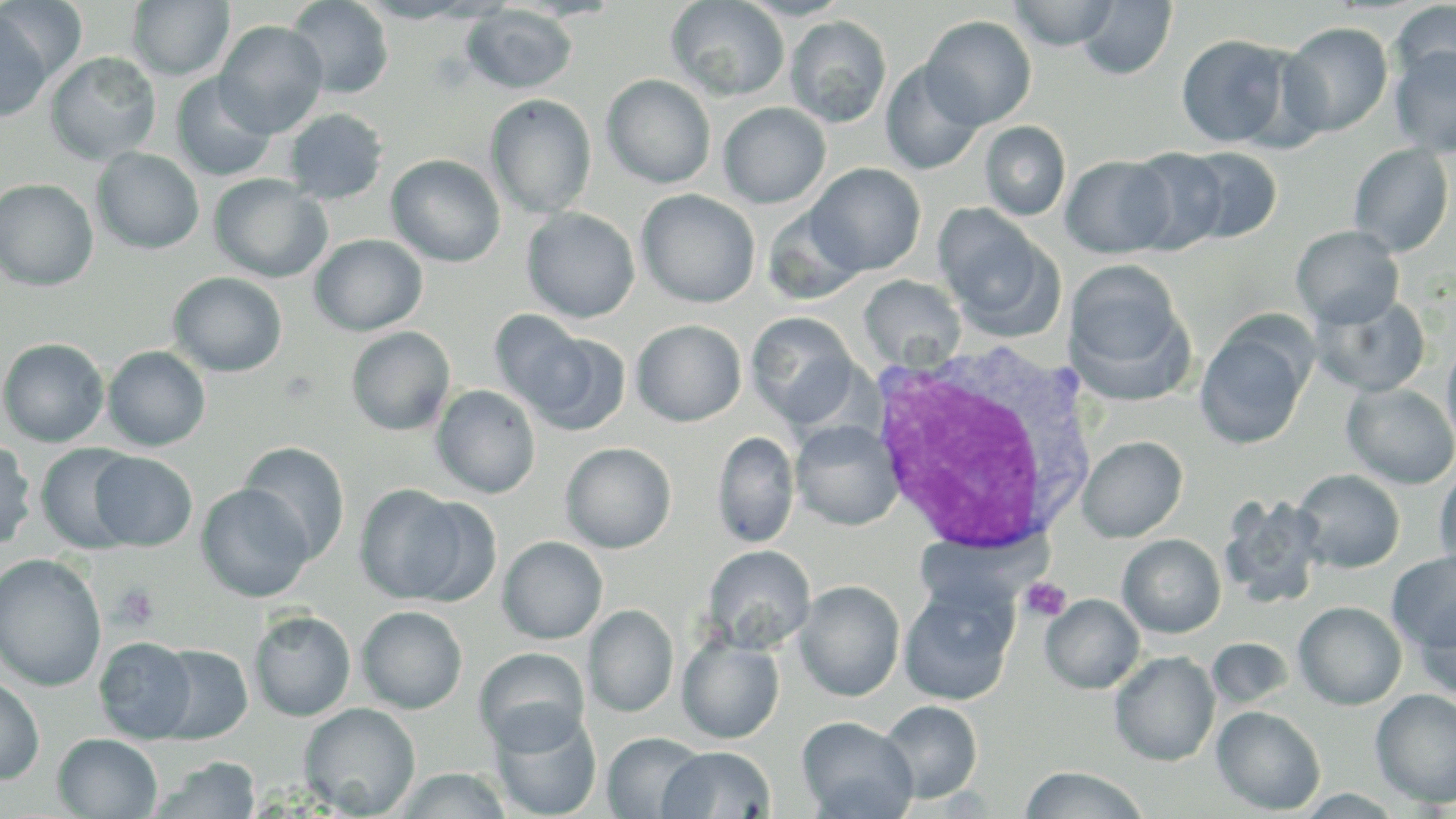

Summary:
  - Coordinate format: approximate bounding boxes as [x1, y1, x2, y2] in pixels
  - Platelet locations: [1019, 577, 1072, 623], [112, 582, 161, 629]
  - Uninfected red blood cell locations: [127, 0, 235, 81], [285, 0, 394, 98], [356, 0, 482, 22], [504, 0, 625, 21], [666, 0, 790, 101], [735, 0, 853, 20], [0, 1, 88, 84], [1009, 1, 1119, 50], [1077, 1, 1177, 80], [1390, 1, 1456, 93], [462, 4, 578, 94], [0, 11, 52, 122], [785, 15, 892, 128], [920, 15, 1037, 129], [214, 20, 329, 138], [1278, 22, 1393, 138], [1175, 33, 1296, 149], [1389, 43, 1456, 158], [45, 52, 161, 164], [880, 60, 985, 175], [171, 73, 277, 182], [601, 74, 716, 189], [486, 95, 596, 218], [718, 102, 831, 208], [283, 108, 389, 204], [980, 121, 1071, 221], [1348, 143, 1455, 257], [1124, 147, 1231, 255], [1177, 147, 1282, 243], [91, 148, 205, 255], [386, 154, 505, 267], [1061, 156, 1174, 258], [806, 163, 926, 275], [209, 174, 331, 283], [0, 178, 98, 289], [636, 189, 760, 308], [933, 204, 1060, 337], [762, 205, 867, 306], [521, 207, 640, 323], [1291, 225, 1405, 329], [310, 234, 428, 336], [1066, 260, 1190, 390], [168, 272, 288, 377], [859, 275, 965, 370], [1309, 293, 1430, 397], [489, 310, 592, 416], [746, 312, 859, 427], [631, 319, 747, 426], [1195, 320, 1313, 451], [346, 326, 455, 436], [524, 330, 631, 436], [1442, 336, 1456, 456], [0, 337, 110, 447], [103, 346, 211, 451], [1341, 382, 1456, 489], [432, 384, 541, 498], [791, 420, 903, 531], [713, 431, 799, 548], [1078, 435, 1187, 542], [0, 439, 36, 551], [238, 441, 351, 563], [36, 442, 142, 554], [560, 442, 676, 553], [89, 452, 198, 551], [1434, 463, 1456, 578], [1291, 469, 1405, 573], [196, 483, 315, 602], [354, 484, 484, 606], [1219, 495, 1327, 609], [1117, 534, 1226, 638], [497, 536, 608, 644], [702, 545, 815, 653], [1387, 551, 1456, 652], [0, 553, 107, 692], [899, 579, 1019, 706], [795, 580, 905, 701], [1040, 594, 1144, 694], [1413, 598, 1456, 703], [1294, 601, 1407, 710], [584, 605, 678, 718], [357, 606, 467, 713], [249, 610, 356, 721], [677, 634, 784, 744], [94, 636, 198, 743], [151, 637, 355, 736], [1207, 637, 1293, 709], [153, 644, 253, 744], [474, 647, 590, 753], [1109, 651, 1220, 766], [0, 676, 44, 785], [1370, 688, 1456, 808], [878, 700, 983, 803], [299, 703, 421, 817], [1212, 705, 1325, 815], [488, 707, 602, 819], [797, 716, 918, 819], [602, 731, 709, 818], [53, 733, 163, 818], [658, 746, 775, 818], [152, 757, 261, 818], [1019, 765, 1150, 819], [393, 767, 514, 818]
  - White blood cell locations: [868, 341, 1099, 557]
  - Slide-level diagnosis: Plasmodium ovale
  - Magnification: 1000x
  - Preparation: thin blood film
  - Modality: optical microscopy
  - Image size: 1456×819 pixels
  - Stain: May-Grünwald-Giemsa
  - Field of view: one of a larger specimen